Assess this cell for malaria.
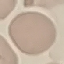
It is uninfected.

capture = smartphone camera at the microscope eyepiece
preparation = thin blood film
stain = Giemsa
image type = automatically extracted cell patch, resized to 64 × 64 pixels